Comment on the morphology of the erythrocytes.
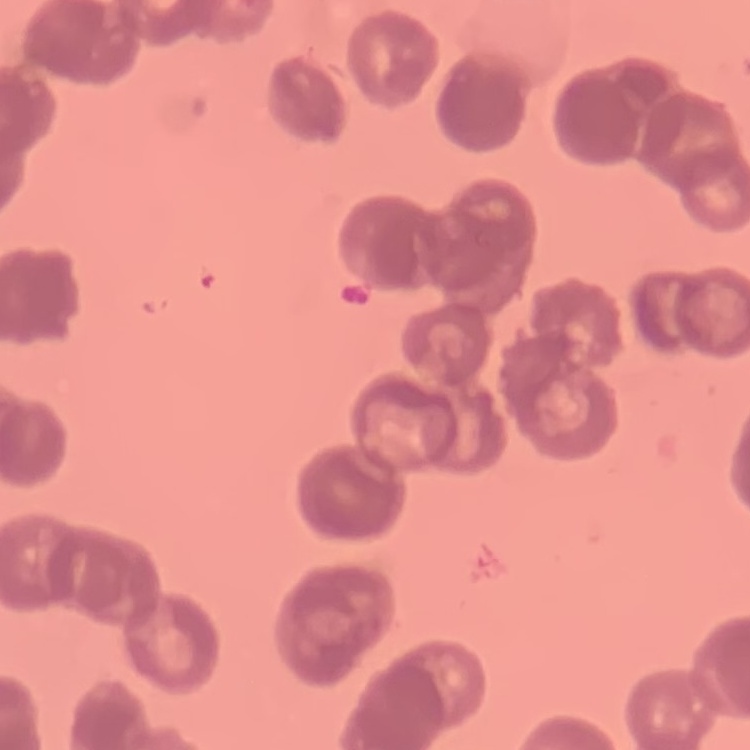
They show rouleaux formation.

{
  "stain": "Field's or Giemsa",
  "image_type": "square crop of a larger photomicrograph",
  "preparation": "thin blood smear"
}